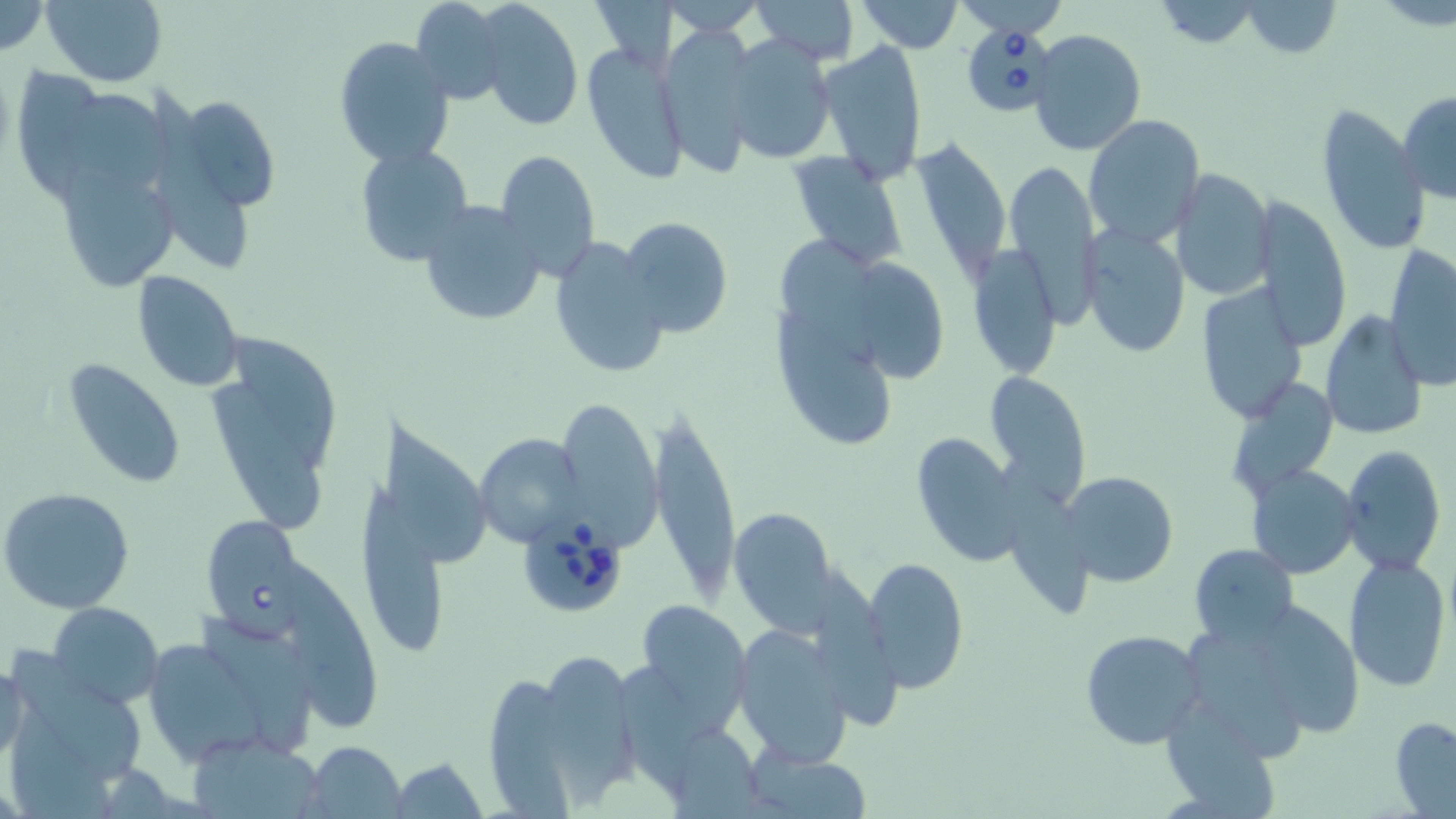
Summary:
  - Coordinate format: approximate bounding boxes as (x1,y1)-(x2,y2) corner pairs in pixels
  - Babesia divergens-infected red blood cell locations: (959,26)-(1059,118), (200,513)-(303,631), (517,518)-(630,621)
  - Uninfected red blood cell locations: (0,0)-(48,57), (41,0)-(166,86), (409,0)-(508,104), (750,0)-(860,63), (856,0)-(963,53), (958,0)-(1063,35), (1149,0)-(1268,50), (1238,0)-(1343,58), (475,1)-(583,130), (661,2)-(766,35), (656,23)-(759,176), (1029,29)-(1146,156), (723,33)-(835,164), (333,37)-(456,169), (581,39)-(691,186), (817,40)-(927,187), (148,90)-(253,273), (1397,90)-(1456,203), (177,93)-(283,212), (78,95)-(181,192), (1315,107)-(1432,257), (1084,114)-(1205,247), (909,140)-(1011,285), (355,143)-(475,269), (496,149)-(601,280), (788,151)-(908,269), (58,157)-(181,293), (1004,157)-(1099,329), (1167,168)-(1273,301), (1252,195)-(1352,353), (418,201)-(548,327), (620,216)-(733,337), (1082,223)-(1189,359), (774,233)-(877,362), (548,236)-(669,382), (1385,242)-(1456,390), (968,246)-(1061,380), (852,256)-(945,383), (132,270)-(245,391), (1193,282)-(1307,423), (774,309)-(896,451), (1320,311)-(1425,441), (205,335)-(343,533), (61,356)-(186,488), (983,369)-(1093,508), (1233,382)-(1339,489), (552,395)-(661,548), (648,398)-(742,606), (378,418)-(492,572), (909,432)-(1027,566), (475,434)-(583,546), (1341,446)-(1446,575), (999,459)-(1086,618), (1248,466)-(1360,579), (1063,470)-(1178,589), (358,480)-(459,654), (0,488)-(134,614), (728,506)-(839,633), (1190,543)-(1297,644), (1343,554)-(1452,692), (865,557)-(969,693), (290,571)-(383,727), (635,599)-(754,730), (1247,599)-(1366,737), (47,601)-(164,710), (194,615)-(310,748), (1184,626)-(1295,759), (731,627)-(854,765), (1081,630)-(1206,749), (139,633)-(288,766), (550,654)-(631,803), (8,655)-(150,802), (0,661)-(29,767), (622,671)-(715,792), (485,676)-(572,819), (1170,696)-(1280,819), (1390,715)-(1456,819), (302,741)-(406,817), (746,749)-(872,818), (390,757)-(488,819)
  - Slide-level diagnosis: Babesia divergens
  - Image size: 1456×819 pixels
  - Stain: May-Grünwald-Giemsa
  - Field of view: single
  - Preparation: thin blood film
  - Modality: light microscopy
  - Magnification: 1000x